Identify the cell.
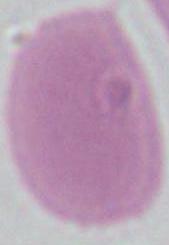

This is an erythrocyte.

Summary:
  - Modality: micrograph
  - Magnification: 1000x